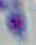

Summary:
  - Identification: Toxoplasma gondii
  - Magnification: 1000x
  - Modality: micrograph